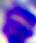

magnification = 400x
modality = photomicrograph
identification = white blood cell